Assess this cell for malaria.
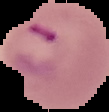
Parasitized.

Summary:
  - Image size: 109×112 pixels
  - Preparation: thin blood film
  - Image type: segmented cell region with the area outside set to black